Locate every blood parasite and identify its species.
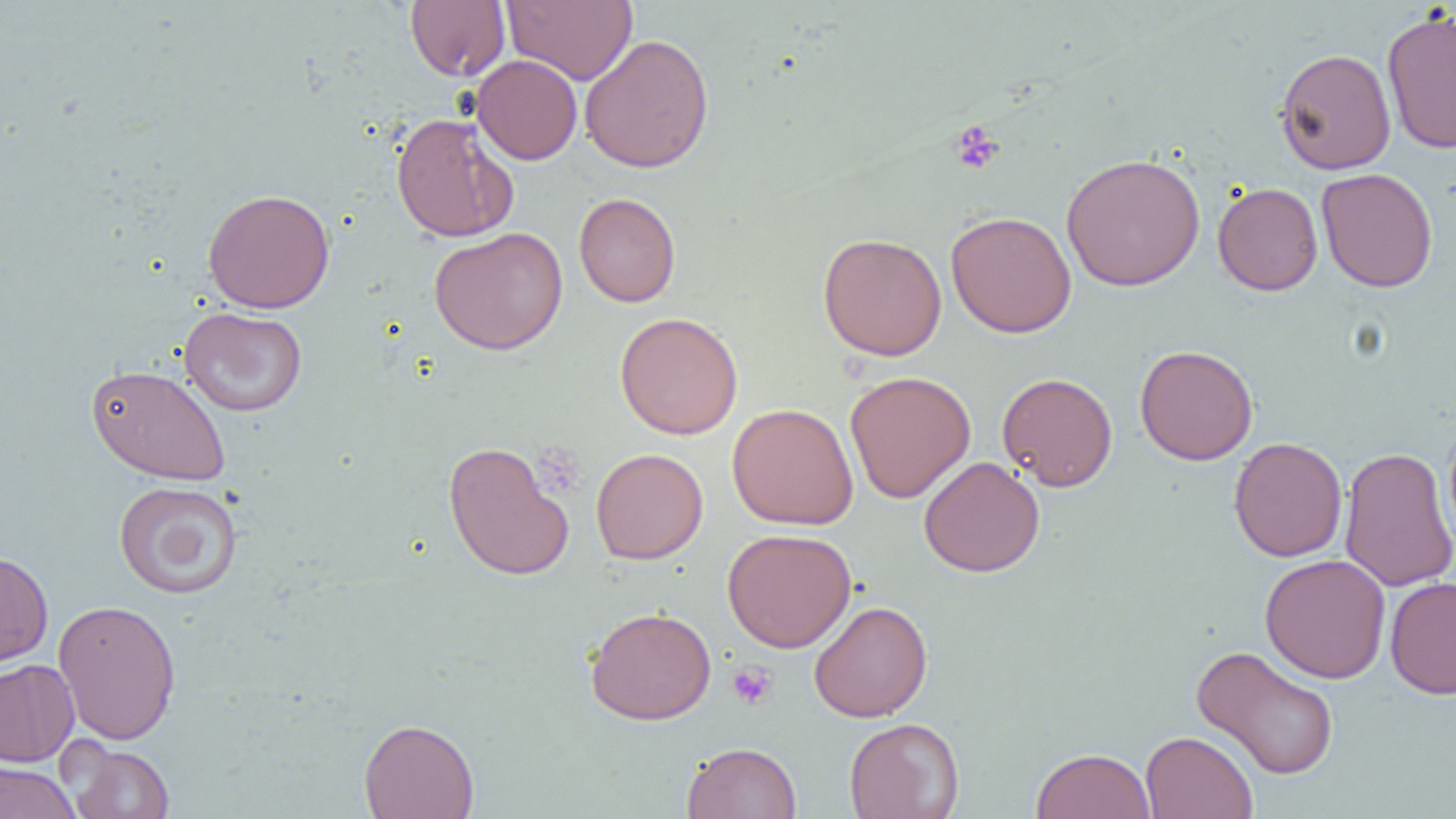

No blood parasites seen.

Approximate bounding boxes as (x1,y1)-(x2,y2) corner pairs in pixels. Platelet locations: (948,119)-(1004,175), (535,439)-(582,494), (727,661)-(778,709). Uninfected red blood cell locations: (502,0)-(638,85), (405,1)-(510,81), (1381,7)-(1456,153), (579,33)-(714,173), (1275,47)-(1396,175), (471,55)-(583,165), (390,112)-(518,243), (1061,152)-(1205,291), (1316,167)-(1438,292), (1212,181)-(1323,296), (203,188)-(335,313), (573,192)-(681,307), (945,210)-(1077,338), (429,227)-(568,354), (818,232)-(947,361), (179,307)-(307,416), (615,311)-(743,439), (1134,344)-(1258,465), (86,363)-(231,486), (845,371)-(976,503), (997,372)-(1118,491), (727,402)-(858,530), (1443,415)-(1456,552), (1228,436)-(1348,562), (443,440)-(574,582), (1339,445)-(1456,593), (591,447)-(708,564), (918,456)-(1045,577), (113,481)-(244,599), (722,528)-(857,652), (0,550)-(53,670), (1260,554)-(1391,683), (1385,576)-(1456,699), (52,598)-(182,745), (808,600)-(933,722), (585,606)-(716,725), (1191,645)-(1341,780), (0,659)-(79,767), (358,717)-(479,819), (844,717)-(964,819), (1141,731)-(1258,819), (61,740)-(176,819), (682,741)-(802,819), (1031,747)-(1157,819), (0,761)-(80,819). Slide-level diagnosis: no evidence of blood parasites. Image is 1456×819 pixels. One field of a larger specimen. Light microscopy. 1000x magnification. Thin blood smear.